Comment on the morphology of the red blood cells.
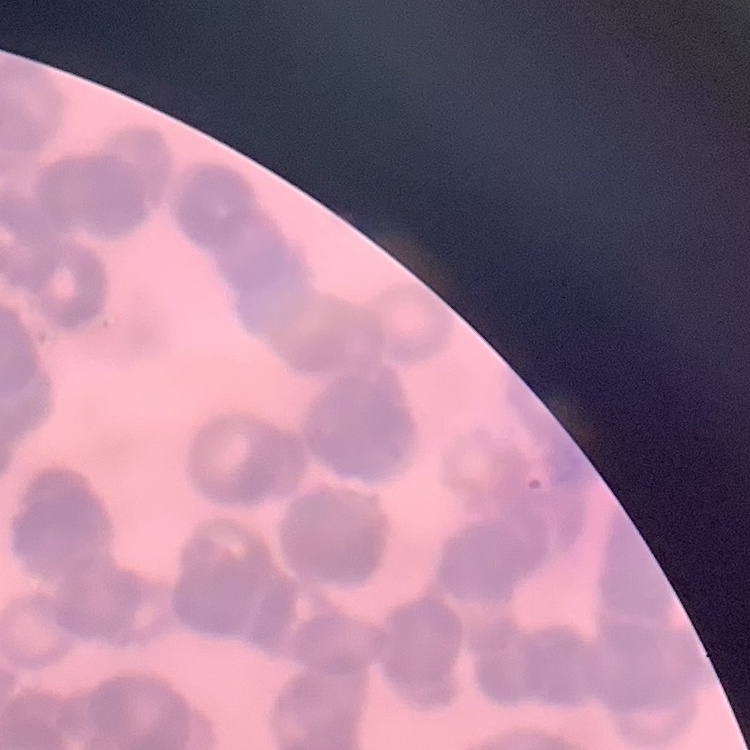

They show rouleaux formation.

image type = one tile cut from a larger photomicrograph
stain = Field's or Giemsa
preparation = thin blood film